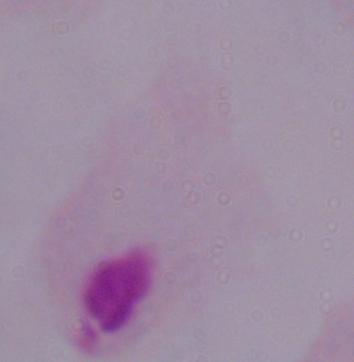
identification: trichomonad
modality: photomicrograph
magnification: 1000x